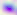
Summary:
  - Modality: photomicrograph
  - Magnification: 400x
  - Identification: Toxoplasma gondii